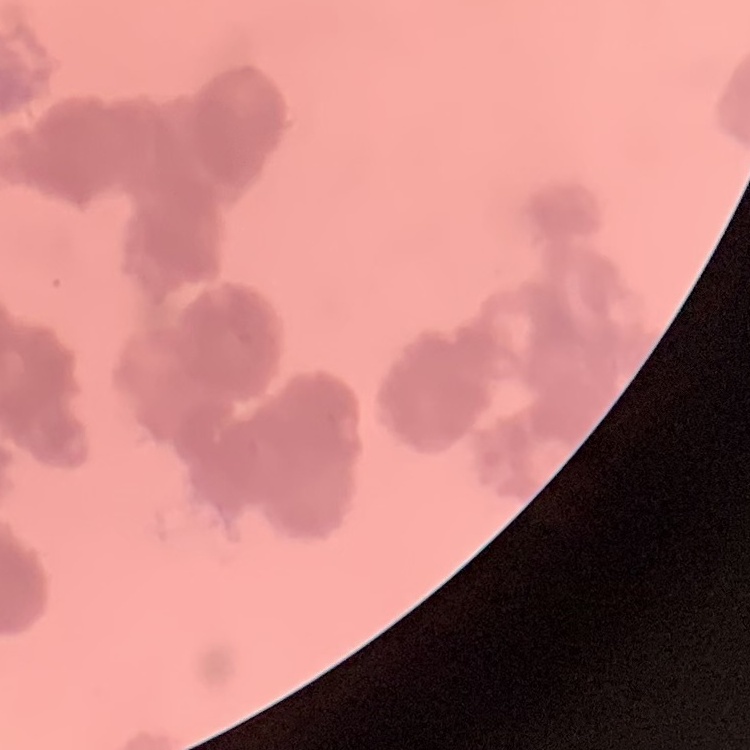
Summary:
  - Erythrocyte morphology: rouleaux formation
  - Preparation: thin peripheral smear
  - Stain: Field's or Giemsa
  - Image type: one tile cut from a larger photomicrograph